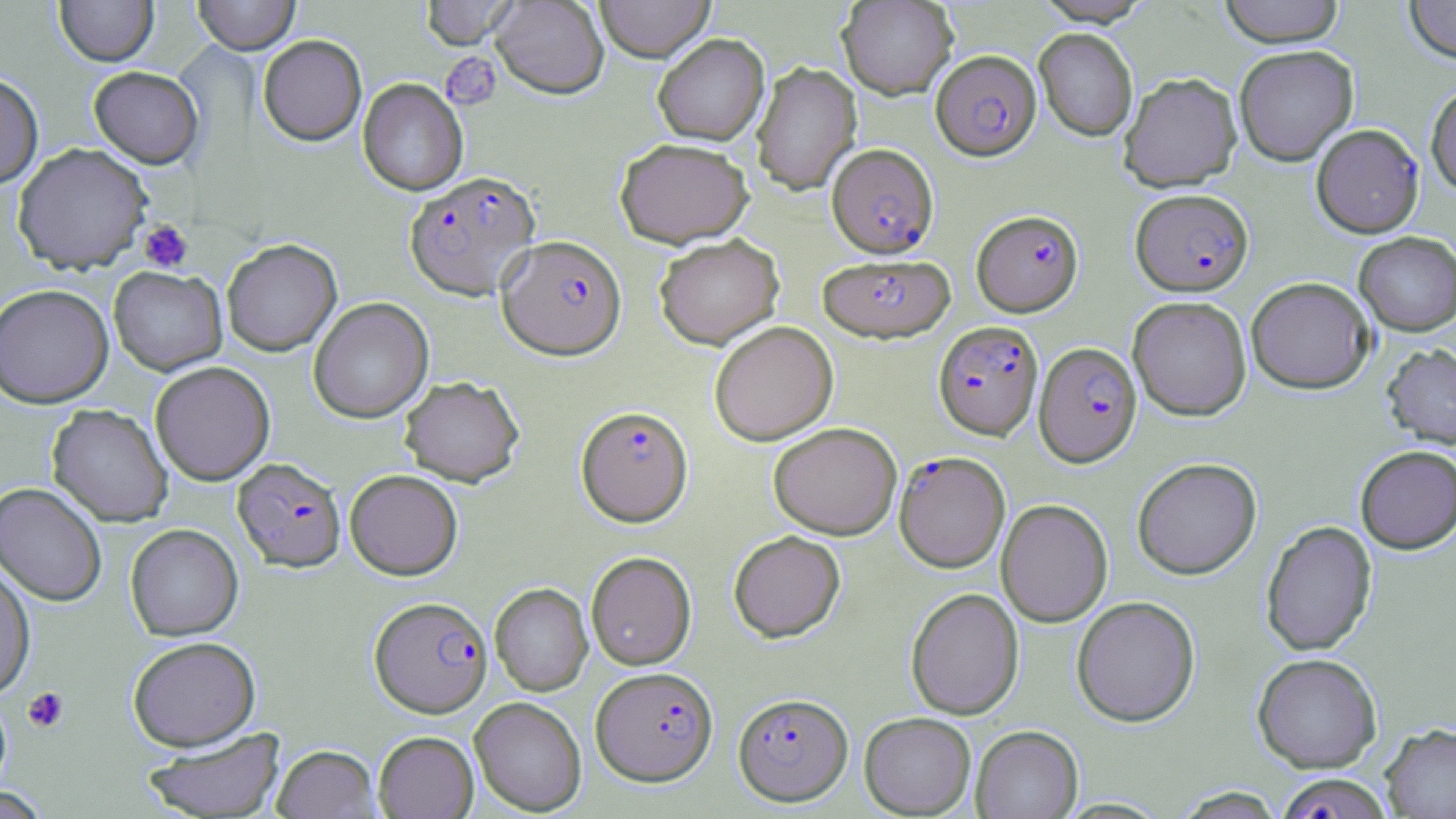
Approximate bounding boxes as (x1,y1)-(x2,y2) corner pairs in pixels. Platelet locations: (440,52)-(501,109), (138,220)-(193,272), (22,686)-(69,733). Plasmodium falciparum-infected red blood cell locations: (931,50)-(1041,162), (1311,123)-(1423,237), (827,145)-(939,259), (405,172)-(540,301), (1131,188)-(1253,296), (972,210)-(1084,317), (497,236)-(626,360), (818,254)-(955,344), (933,321)-(1043,441), (1034,342)-(1142,467), (576,406)-(693,527), (894,451)-(1010,573), (233,458)-(346,571), (369,596)-(492,717), (591,666)-(718,786), (733,692)-(853,806), (1273,773)-(1395,818). Uninfected red blood cell locations: (54,0)-(158,66), (192,0)-(300,55), (419,0)-(519,50), (491,0)-(609,100), (594,0)-(715,64), (837,0)-(958,99), (1032,0)-(1154,26), (1218,0)-(1345,48), (1404,0)-(1456,63), (1034,29)-(1138,142), (258,35)-(367,146), (653,35)-(769,148), (1234,45)-(1358,166), (752,62)-(862,196), (88,66)-(204,168), (0,72)-(43,188), (1118,72)-(1242,192), (358,79)-(468,196), (1426,83)-(1456,196), (616,140)-(754,249), (13,142)-(153,273), (1354,231)-(1456,335), (654,235)-(784,349), (222,239)-(342,356), (108,266)-(227,376), (1246,277)-(1374,393), (0,284)-(114,408), (1127,296)-(1252,421), (308,297)-(434,423), (709,322)-(838,446), (1382,343)-(1456,449), (150,361)-(275,486), (399,376)-(524,487), (47,405)-(173,527), (769,422)-(901,540), (1355,445)-(1456,553), (1132,457)-(1262,579), (345,469)-(463,579), (0,482)-(108,606), (996,499)-(1113,627), (1260,520)-(1377,656), (125,523)-(243,640), (729,531)-(845,643), (586,551)-(696,670), (0,560)-(36,701), (490,583)-(592,696), (906,588)-(1024,720), (1071,596)-(1200,727), (127,636)-(260,750), (1252,652)-(1382,773), (470,697)-(586,815), (859,712)-(976,817), (1381,723)-(1456,818), (971,725)-(1084,819), (142,727)-(286,818), (374,731)-(478,818), (272,744)-(382,818). Slide-level diagnosis: Plasmodium falciparum. One field of a larger specimen. May-Grünwald-Giemsa-stained preparation. Optical microscopy. Thin blood film. 1000x magnification. Image is 1456×819 pixels.